Report the malaria status.
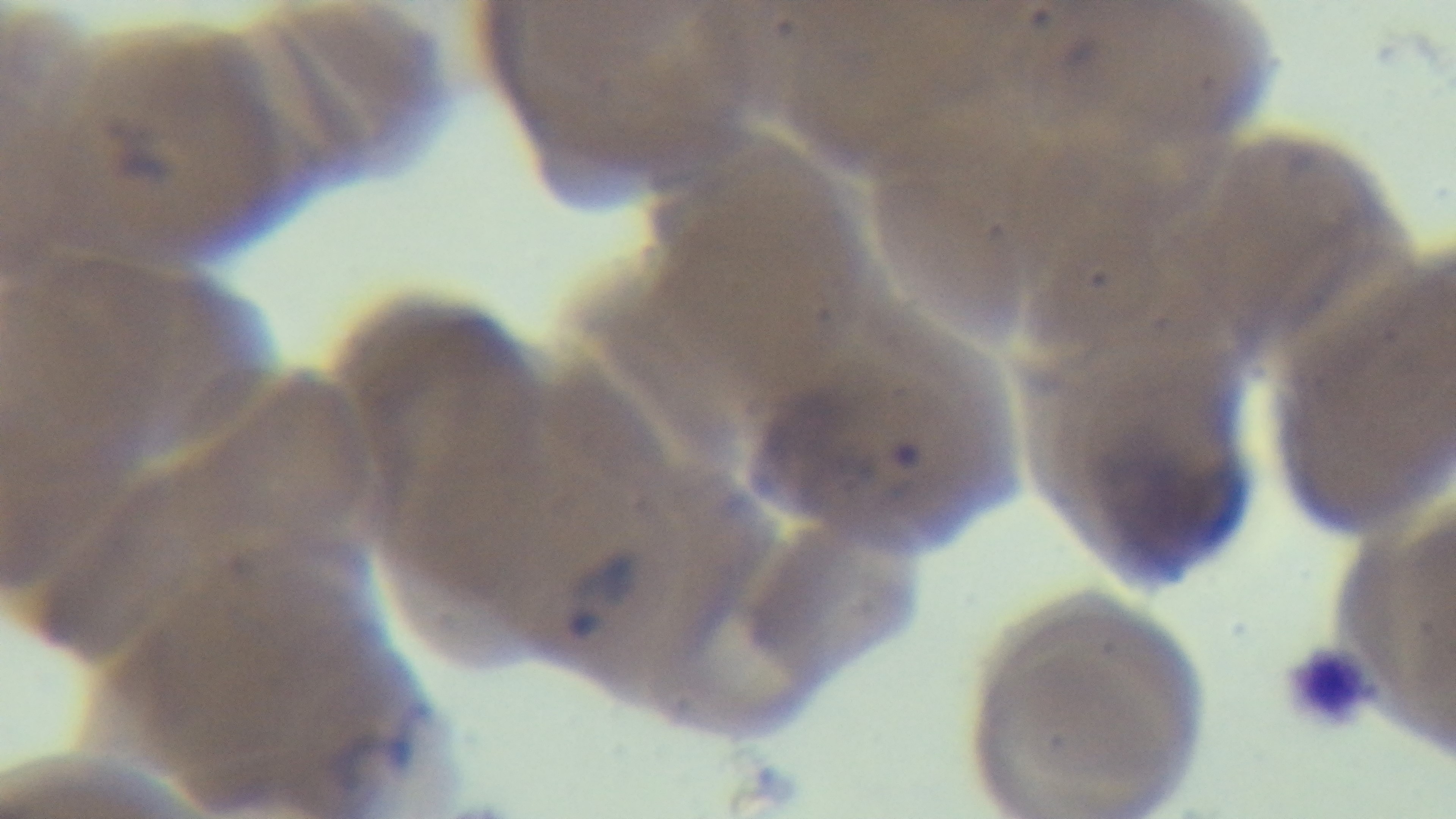

It is infected.

modality = light microscopy
preparation = thin smear
objective = 100x oil immersion
stain = Giemsa
capture = mounted 4K digital camera
field of view = single